Outline each Plasmodium ovale-infected red blood cell.
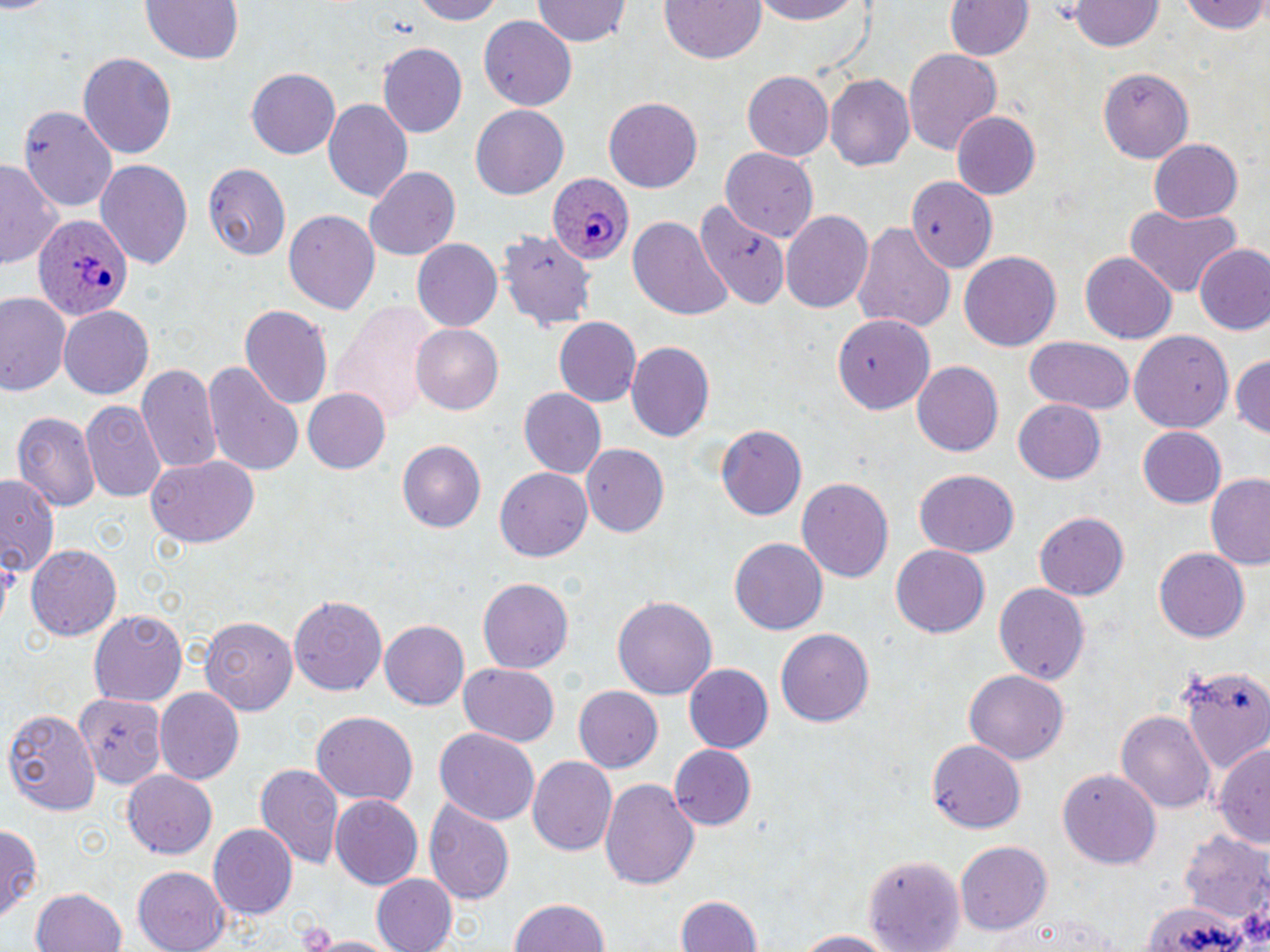
Approximate bounding boxes as (x1, y1, x2, y2) in pixels.
Plasmodium ovale-infected red blood cells: (548, 176, 636, 262), (34, 215, 133, 323).

{
  "slide_level_diagnosis": "Plasmodium ovale",
  "magnification": "1000x",
  "image_size": "1270×952 pixels",
  "modality": "optical microscopy",
  "preparation": "thin blood smear",
  "stain": "May-Grünwald-Giemsa",
  "uninfected_red_blood_cell_locations": "approximate bounding boxes as (x1, y1, x2, y2) in pixels: (135, 0, 249, 66), (408, 0, 504, 23), (658, 0, 769, 66), (751, 0, 864, 24), (0, 1, 53, 17), (532, 1, 630, 47), (946, 1, 1032, 61), (1072, 1, 1162, 52), (1183, 1, 1270, 36), (479, 16, 579, 110), (378, 42, 467, 136), (901, 46, 1002, 156), (76, 50, 176, 161), (1098, 66, 1194, 164), (245, 67, 339, 159), (741, 72, 833, 162), (826, 75, 914, 172), (604, 96, 704, 191), (325, 98, 413, 203), (470, 104, 568, 198), (18, 105, 118, 212), (951, 111, 1041, 198), (1149, 138, 1244, 223), (720, 147, 819, 242), (95, 159, 195, 270), (0, 162, 60, 271), (201, 162, 290, 262), (362, 165, 463, 261), (908, 177, 996, 273), (695, 201, 790, 312), (1123, 205, 1243, 295), (285, 208, 380, 315), (782, 209, 874, 314), (628, 216, 730, 318), (852, 218, 955, 335), (499, 227, 596, 332), (413, 240, 502, 332), (1194, 245, 1269, 335), (959, 252, 1063, 350), (1079, 254, 1175, 343), (0, 290, 70, 396), (330, 301, 440, 425), (240, 303, 334, 411), (60, 307, 153, 399), (833, 310, 933, 411), (551, 317, 642, 408), (409, 324, 504, 415), (1130, 329, 1234, 436), (1023, 336, 1136, 415), (627, 341, 716, 443), (1230, 350, 1270, 439), (202, 361, 306, 475), (912, 361, 1004, 458), (138, 364, 223, 475), (304, 389, 390, 473), (519, 389, 607, 480), (1013, 399, 1106, 484), (79, 403, 165, 502), (11, 413, 99, 510), (713, 422, 806, 520), (1137, 427, 1227, 509), (397, 442, 486, 534), (581, 444, 669, 536), (146, 454, 260, 549), (497, 468, 592, 563), (914, 468, 1019, 557), (1205, 475, 1270, 570), (797, 476, 894, 583), (2, 478, 59, 579), (1033, 511, 1130, 601), (729, 538, 826, 633), (26, 545, 121, 642), (892, 545, 990, 637), (1153, 547, 1250, 642), (479, 577, 575, 674), (993, 581, 1090, 684), (290, 593, 387, 697), (612, 593, 719, 700), (88, 610, 187, 706), (200, 616, 297, 715), (378, 619, 467, 712), (775, 628, 877, 727), (458, 663, 560, 748), (682, 663, 773, 755), (1178, 666, 1269, 773), (962, 668, 1071, 766), (574, 686, 663, 773), (154, 689, 244, 785), (76, 692, 164, 790), (2, 706, 100, 815), (1117, 709, 1216, 813), (310, 712, 419, 807), (434, 725, 538, 824), (928, 739, 1024, 834), (1216, 739, 1269, 853), (668, 745, 755, 832), (530, 756, 620, 855), (255, 765, 343, 872), (122, 768, 217, 861), (1057, 768, 1162, 869), (601, 777, 698, 892), (328, 795, 423, 889), (425, 799, 514, 907), (0, 824, 41, 924), (209, 825, 297, 918), (1182, 831, 1269, 922), (957, 840, 1054, 936), (864, 853, 966, 949), (132, 868, 230, 952), (372, 874, 459, 952), (31, 887, 127, 952), (670, 893, 763, 952), (509, 898, 611, 952), (1145, 899, 1255, 951), (993, 910, 1127, 952), (789, 930, 901, 950), (305, 933, 408, 952)",
  "platelet_locations": "approximate bounding boxes as (x1, y1, x2, y2) in pixels: (1242, 911, 1270, 948)",
  "field_of_view": "single"
}